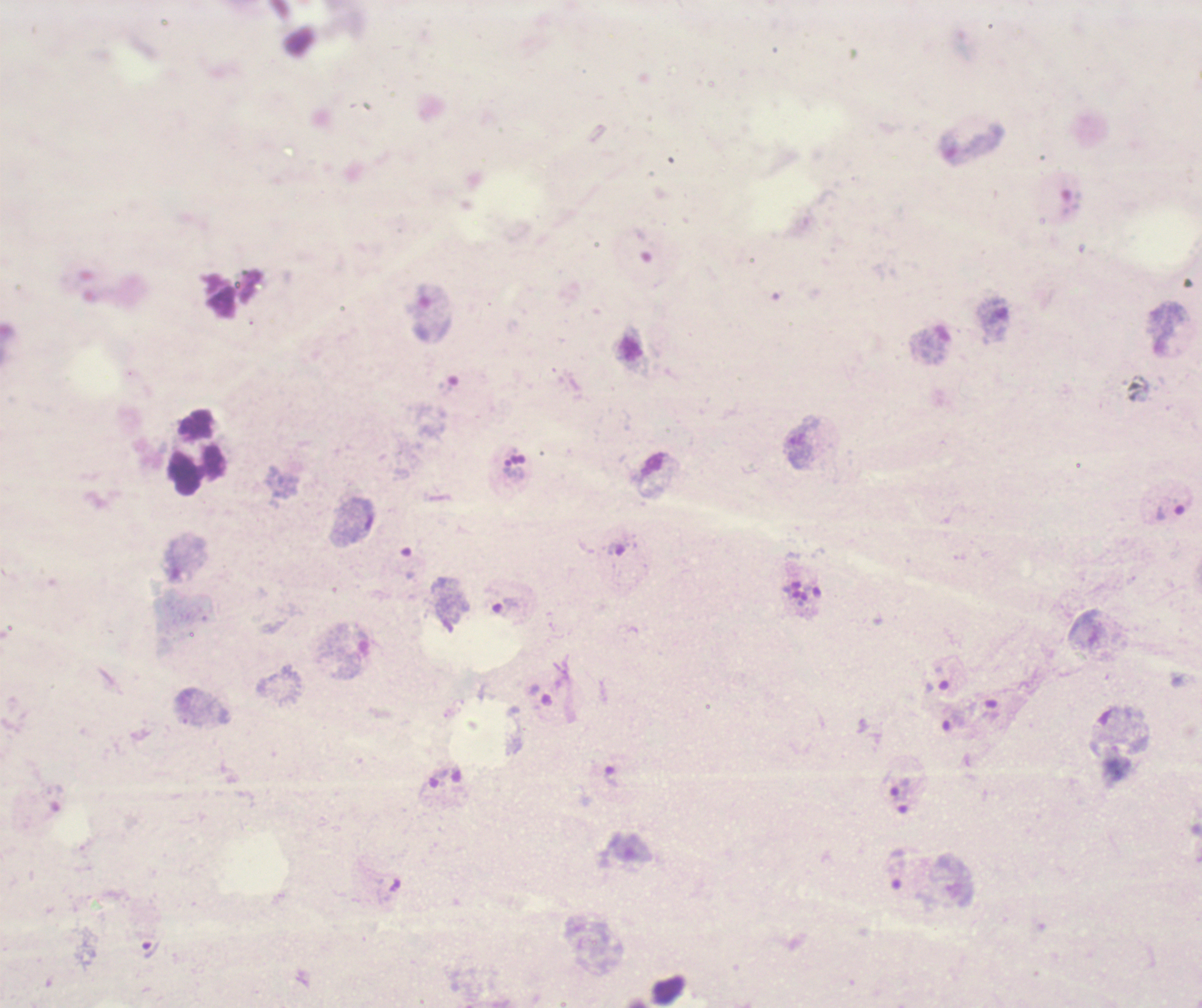

coloration_quality: bad
result: Plasmodium parasites detected
background_quality: poor
trophozoite_locations: 'approximate centers as [x, y] in pixels: [510, 471], [1170, 514], [616, 551], [791, 587], [505, 607], [611, 778], [439, 780], [901, 790], [150, 950]'
leukocyte_locations: 'approximate centers as [x, y] in pixels: [198, 452]'
field_of_view: single
image_size: 1202×1008 pixels
stain: Romanowsky
magnification: 100x
context: previously used in an actual diagnosis
preparation: thick smear of blood